Classify this cell by malaria status.
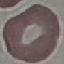

It is uninfected.

Thin blood smear. Acquired by smartphone through the microscope eyepiece. Cell patch, automatically extracted from a larger field of view and resized to 64 × 64 pixels. Giemsa-stained preparation.